Outline each blood parasite and name the species.
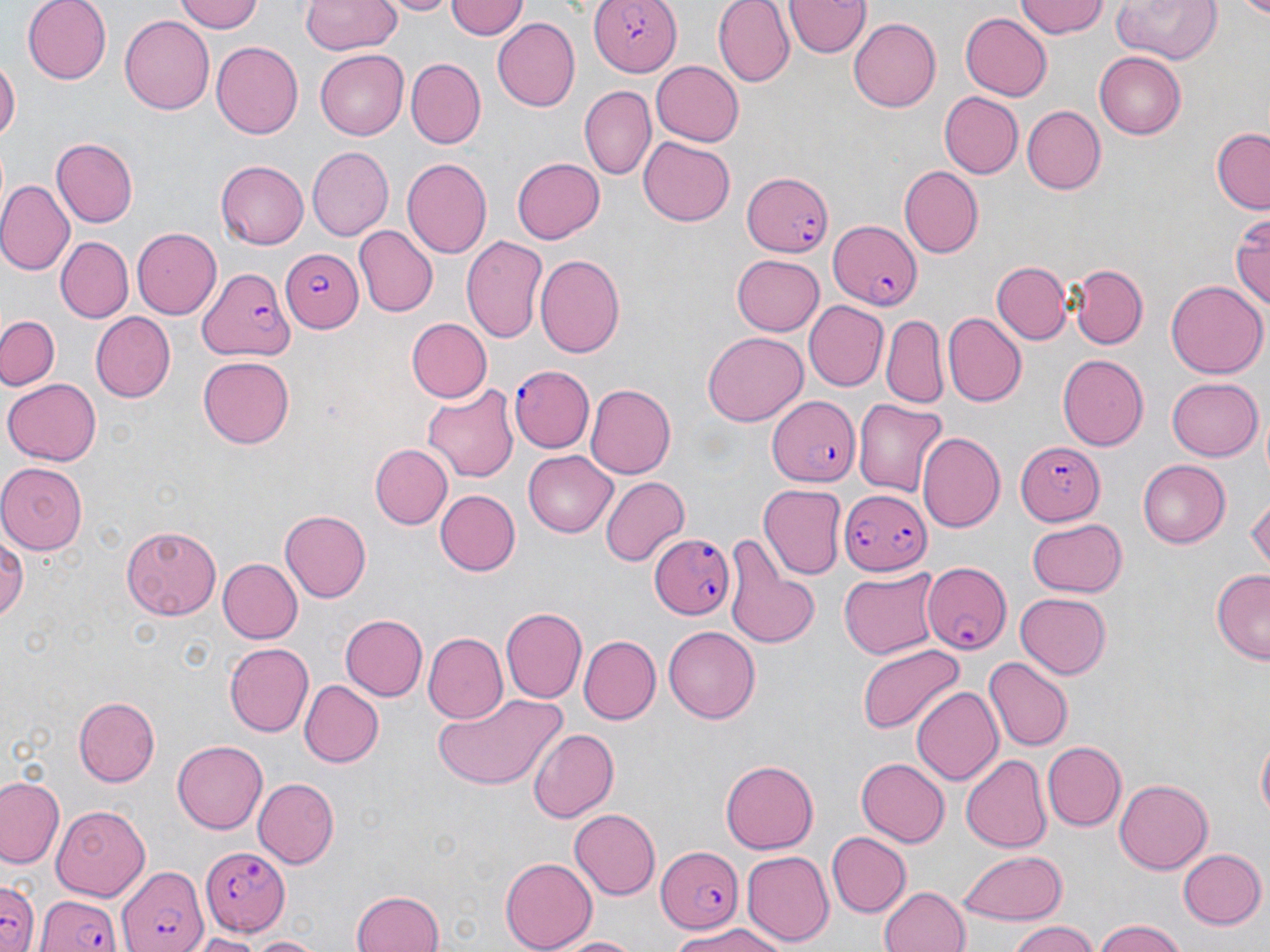

Approximate bounding boxes as named x1/y1/x2/y2 corners in pixels.
Plasmodium falciparum-infected red blood cells: (x1=588, y1=0, x2=682, y2=76), (x1=743, y1=169, x2=836, y2=258), (x1=828, y1=219, x2=922, y2=311), (x1=281, y1=252, x2=364, y2=333), (x1=197, y1=264, x2=294, y2=363), (x1=509, y1=365, x2=594, y2=452), (x1=766, y1=396, x2=862, y2=485), (x1=1017, y1=438, x2=1107, y2=525), (x1=840, y1=489, x2=928, y2=572), (x1=648, y1=536, x2=738, y2=618), (x1=921, y1=559, x2=1009, y2=654), (x1=203, y1=844, x2=291, y2=935), (x1=653, y1=845, x2=747, y2=934), (x1=113, y1=860, x2=208, y2=952), (x1=0, y1=879, x2=40, y2=952), (x1=34, y1=892, x2=127, y2=952).
No Plasmodium ovale, Plasmodium malariae, Plasmodium vivax, Babesia divergens, or Trypanosoma brucei observed.

Uninfected red blood cell locations: (x1=25, y1=0, x2=111, y2=83), (x1=176, y1=0, x2=265, y2=33), (x1=387, y1=0, x2=456, y2=16), (x1=445, y1=0, x2=528, y2=42), (x1=713, y1=0, x2=795, y2=87), (x1=1017, y1=0, x2=1109, y2=41), (x1=1109, y1=0, x2=1221, y2=64), (x1=1230, y1=0, x2=1270, y2=18), (x1=299, y1=1, x2=400, y2=55), (x1=784, y1=1, x2=868, y2=58), (x1=960, y1=11, x2=1052, y2=100), (x1=120, y1=15, x2=214, y2=114), (x1=848, y1=17, x2=942, y2=111), (x1=492, y1=18, x2=581, y2=112), (x1=212, y1=42, x2=303, y2=139), (x1=315, y1=50, x2=407, y2=140), (x1=1093, y1=53, x2=1185, y2=141), (x1=408, y1=58, x2=487, y2=147), (x1=0, y1=60, x2=19, y2=145), (x1=649, y1=60, x2=744, y2=148), (x1=580, y1=85, x2=656, y2=181), (x1=937, y1=92, x2=1022, y2=179), (x1=1023, y1=106, x2=1104, y2=194), (x1=1211, y1=129, x2=1270, y2=212), (x1=639, y1=136, x2=735, y2=225), (x1=53, y1=137, x2=140, y2=228), (x1=307, y1=147, x2=392, y2=240), (x1=511, y1=156, x2=604, y2=245), (x1=403, y1=158, x2=492, y2=259), (x1=215, y1=161, x2=308, y2=249), (x1=900, y1=167, x2=983, y2=259), (x1=0, y1=183, x2=73, y2=274), (x1=1231, y1=212, x2=1269, y2=314), (x1=353, y1=226, x2=437, y2=316), (x1=132, y1=228, x2=223, y2=318), (x1=460, y1=233, x2=549, y2=343), (x1=56, y1=236, x2=133, y2=324), (x1=533, y1=254, x2=624, y2=360), (x1=733, y1=254, x2=825, y2=336), (x1=992, y1=261, x2=1070, y2=344), (x1=1066, y1=263, x2=1148, y2=350), (x1=1166, y1=279, x2=1266, y2=380), (x1=804, y1=301, x2=888, y2=391), (x1=89, y1=312, x2=176, y2=402), (x1=943, y1=312, x2=1024, y2=405), (x1=0, y1=315, x2=62, y2=389), (x1=882, y1=315, x2=946, y2=408), (x1=406, y1=318, x2=492, y2=403), (x1=704, y1=329, x2=806, y2=423), (x1=1057, y1=353, x2=1149, y2=452), (x1=199, y1=355, x2=294, y2=449), (x1=4, y1=377, x2=100, y2=466), (x1=1166, y1=377, x2=1263, y2=460), (x1=585, y1=383, x2=676, y2=479), (x1=421, y1=386, x2=518, y2=483), (x1=853, y1=398, x2=948, y2=496), (x1=917, y1=431, x2=1005, y2=534), (x1=368, y1=443, x2=451, y2=529), (x1=522, y1=452, x2=617, y2=537), (x1=1136, y1=460, x2=1229, y2=547), (x1=1, y1=462, x2=85, y2=552), (x1=599, y1=476, x2=688, y2=566), (x1=757, y1=485, x2=846, y2=581), (x1=437, y1=489, x2=521, y2=576), (x1=1248, y1=497, x2=1269, y2=569), (x1=279, y1=509, x2=370, y2=602), (x1=1025, y1=518, x2=1129, y2=596), (x1=123, y1=524, x2=221, y2=620), (x1=0, y1=531, x2=26, y2=627), (x1=724, y1=542, x2=820, y2=653), (x1=217, y1=558, x2=302, y2=644), (x1=838, y1=567, x2=942, y2=659), (x1=1210, y1=569, x2=1270, y2=663), (x1=1015, y1=592, x2=1111, y2=678), (x1=502, y1=606, x2=586, y2=703), (x1=341, y1=614, x2=427, y2=701), (x1=664, y1=625, x2=759, y2=723), (x1=424, y1=632, x2=508, y2=725), (x1=579, y1=636, x2=660, y2=722), (x1=225, y1=642, x2=313, y2=737), (x1=857, y1=643, x2=963, y2=734), (x1=982, y1=657, x2=1071, y2=752), (x1=298, y1=678, x2=383, y2=767), (x1=912, y1=687, x2=1003, y2=786), (x1=432, y1=692, x2=568, y2=790), (x1=73, y1=696, x2=160, y2=786), (x1=527, y1=727, x2=620, y2=822), (x1=1255, y1=733, x2=1270, y2=820), (x1=171, y1=740, x2=267, y2=834), (x1=1043, y1=741, x2=1126, y2=831), (x1=961, y1=754, x2=1052, y2=854), (x1=856, y1=756, x2=948, y2=846), (x1=720, y1=760, x2=818, y2=855), (x1=0, y1=776, x2=64, y2=870), (x1=251, y1=778, x2=337, y2=869), (x1=1114, y1=778, x2=1214, y2=873), (x1=52, y1=804, x2=150, y2=899), (x1=569, y1=809, x2=661, y2=899), (x1=826, y1=832, x2=909, y2=917), (x1=1178, y1=847, x2=1266, y2=930), (x1=958, y1=849, x2=1067, y2=924), (x1=741, y1=850, x2=832, y2=946), (x1=499, y1=856, x2=596, y2=952), (x1=879, y1=884, x2=971, y2=952), (x1=351, y1=888, x2=446, y2=952), (x1=1091, y1=920, x2=1187, y2=952), (x1=671, y1=922, x2=788, y2=952), (x1=1007, y1=922, x2=1104, y2=952), (x1=191, y1=932, x2=267, y2=951), (x1=243, y1=934, x2=323, y2=952), (x1=554, y1=935, x2=643, y2=952). Slide-level diagnosis: Plasmodium falciparum. Light microscopy. 1000x magnification. One field of a larger specimen. Image is 1270×952 pixels. May-Grünwald-Giemsa stain. Thin blood film.